Classify this cell by malaria status.
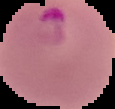
Parasitized.

image type = cell region segmented out of the field of view; surrounding area masked to black
preparation = thin blood film
image size = 115×109 pixels